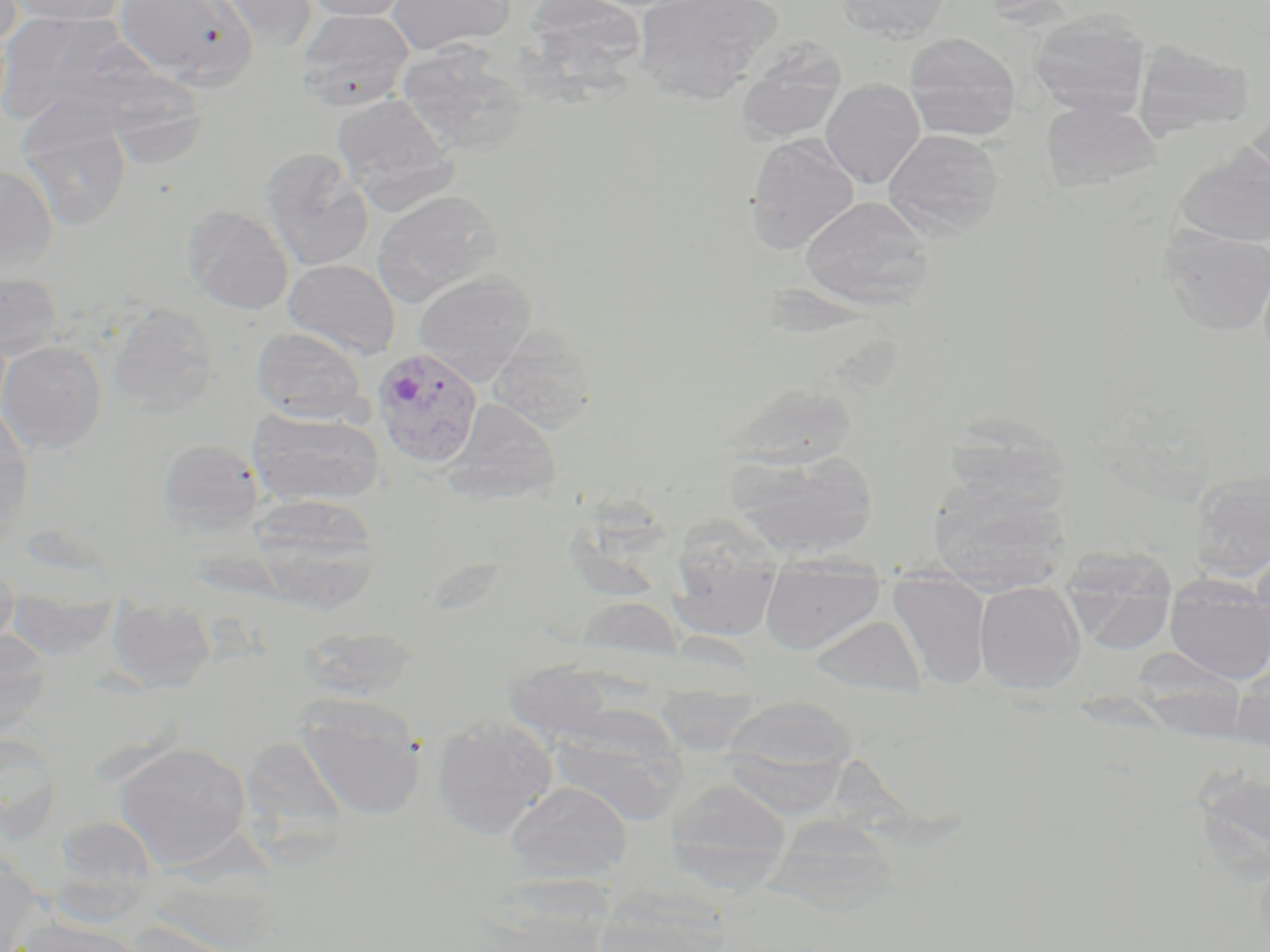
Approximate bounding boxes as [x1, y1, x2, y2] in pixels. Uninfected red blood cell locations: [4, 0, 128, 25], [115, 0, 257, 86], [209, 0, 319, 50], [302, 0, 412, 21], [387, 0, 515, 54], [529, 0, 646, 112], [633, 0, 783, 100], [836, 0, 954, 41], [296, 9, 413, 112], [0, 11, 135, 125], [1029, 13, 1151, 118], [904, 33, 1021, 139], [736, 38, 847, 145], [1133, 39, 1255, 140], [397, 44, 526, 156], [101, 69, 209, 168], [820, 79, 925, 189], [333, 93, 458, 211], [1042, 99, 1161, 192], [18, 102, 133, 231], [1242, 110, 1270, 200], [884, 129, 1005, 238], [745, 134, 859, 252], [1177, 147, 1270, 248], [260, 149, 374, 272], [0, 164, 58, 276], [372, 190, 502, 303], [799, 196, 934, 307], [182, 206, 294, 313], [1159, 227, 1270, 336], [284, 259, 400, 359], [0, 270, 64, 360], [413, 270, 536, 385], [108, 303, 219, 415], [488, 326, 596, 434], [250, 327, 368, 423], [0, 340, 107, 453], [725, 383, 860, 470], [445, 399, 560, 501], [0, 405, 34, 541], [247, 408, 384, 508], [943, 416, 1071, 513], [157, 438, 263, 537], [728, 449, 879, 558], [1188, 473, 1270, 585], [928, 477, 1069, 593], [249, 495, 382, 613], [667, 518, 784, 643], [1060, 546, 1179, 654], [760, 557, 884, 655], [0, 560, 18, 650], [888, 571, 991, 689], [1165, 575, 1270, 684], [974, 581, 1086, 693], [7, 588, 121, 659], [574, 596, 684, 668], [108, 600, 216, 692], [809, 614, 926, 697], [298, 625, 417, 703], [0, 631, 53, 737], [1131, 651, 1250, 740], [504, 659, 617, 743], [1230, 663, 1270, 750], [722, 695, 858, 785], [294, 696, 426, 821], [548, 711, 687, 825], [430, 716, 557, 839], [0, 729, 62, 842], [113, 742, 252, 869], [666, 778, 793, 885], [505, 781, 632, 883], [51, 815, 160, 913], [765, 815, 900, 917], [0, 860, 46, 950], [591, 900, 731, 951], [13, 917, 146, 952], [126, 920, 262, 952]. Plasmodium vivax-infected red blood cell locations: [371, 347, 484, 468]. Slide-level diagnosis: Plasmodium vivax. Image is 1270×952 pixels. May-Grünwald-Giemsa stain. 1000x magnification. One field of a larger specimen. Thin blood film. Optical microscopy.